State which parasite is depicted.
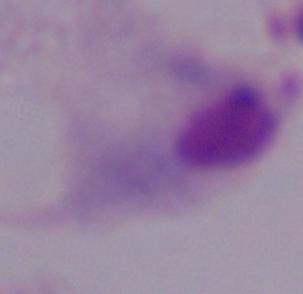

A trichomonad.

magnification = 1000x
modality = micrograph